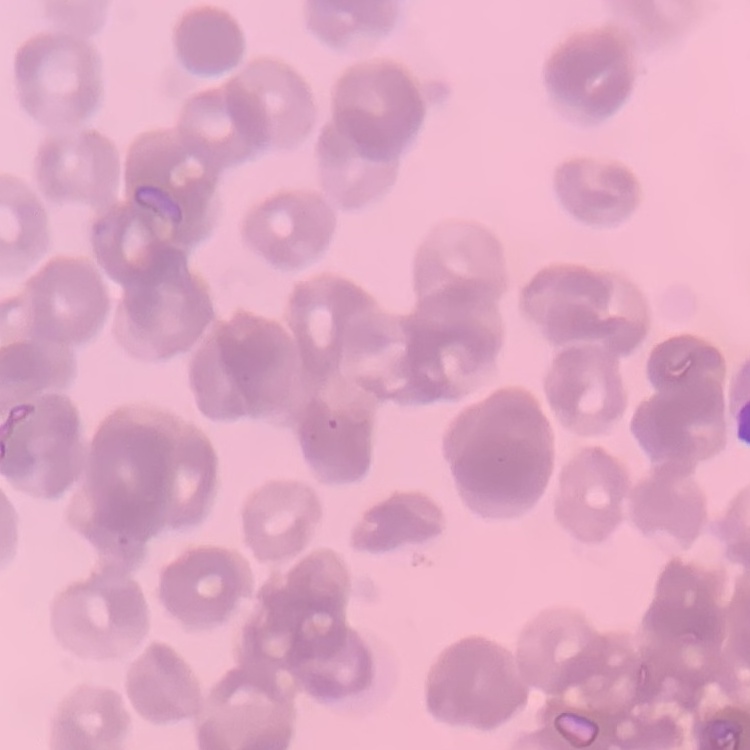
{
  "red_blood_cell_morphology": "rouleaux formation",
  "stain": "Field's or Giemsa",
  "preparation": "thin blood film",
  "image_type": "one tile cut from a larger photomicrograph"
}